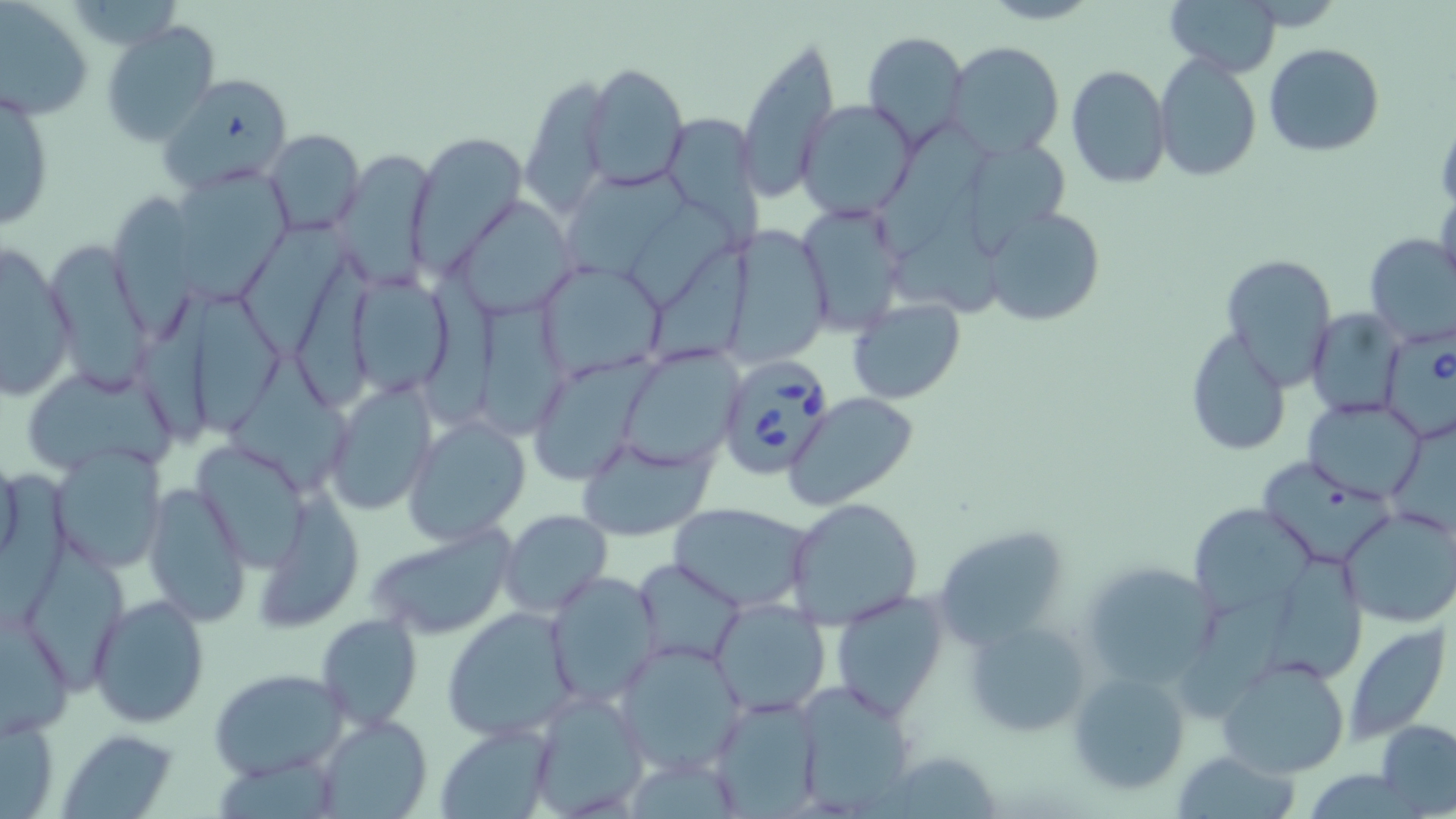
Babesia divergens-infected red blood cell locations = approximate bounding boxes as named x1/y1/x2/y2 corners in pixels: (x1=1383, y1=330, x2=1455, y2=452), (x1=715, y1=356, x2=837, y2=481)
slide-level diagnosis = Babesia divergens
image size = 1456×819 pixels
uninfected red blood cell locations = approximate bounding boxes as named x1/y1/x2/y2 corners in pixels: (x1=1164, y1=0, x2=1279, y2=74), (x1=0, y1=1, x2=93, y2=120), (x1=101, y1=20, x2=222, y2=145), (x1=862, y1=30, x2=969, y2=146), (x1=735, y1=36, x2=839, y2=202), (x1=944, y1=40, x2=1065, y2=158), (x1=1264, y1=43, x2=1385, y2=156), (x1=1154, y1=53, x2=1262, y2=183), (x1=582, y1=63, x2=689, y2=188), (x1=1066, y1=64, x2=1170, y2=189), (x1=159, y1=73, x2=293, y2=190), (x1=519, y1=80, x2=610, y2=213), (x1=0, y1=83, x2=55, y2=235), (x1=797, y1=100, x2=916, y2=219), (x1=671, y1=110, x2=769, y2=238), (x1=875, y1=121, x2=988, y2=251), (x1=263, y1=128, x2=366, y2=239), (x1=406, y1=132, x2=525, y2=274), (x1=967, y1=141, x2=1065, y2=254), (x1=329, y1=150, x2=437, y2=290), (x1=168, y1=168, x2=294, y2=300), (x1=1435, y1=182, x2=1456, y2=297), (x1=110, y1=190, x2=195, y2=340), (x1=625, y1=196, x2=739, y2=302), (x1=455, y1=197, x2=575, y2=315), (x1=984, y1=206, x2=1107, y2=329), (x1=800, y1=207, x2=905, y2=343), (x1=243, y1=210, x2=350, y2=353), (x1=719, y1=228, x2=828, y2=362), (x1=1364, y1=234, x2=1455, y2=346), (x1=1, y1=240, x2=78, y2=401), (x1=45, y1=241, x2=152, y2=389), (x1=1222, y1=253, x2=1338, y2=383), (x1=537, y1=262, x2=663, y2=381), (x1=349, y1=269, x2=454, y2=401), (x1=136, y1=289, x2=215, y2=447), (x1=194, y1=292, x2=283, y2=440), (x1=847, y1=297, x2=965, y2=404), (x1=1305, y1=309, x2=1405, y2=416), (x1=1185, y1=329, x2=1293, y2=457), (x1=229, y1=346, x2=349, y2=494), (x1=621, y1=347, x2=745, y2=468), (x1=527, y1=357, x2=654, y2=486), (x1=21, y1=364, x2=177, y2=480), (x1=323, y1=385, x2=437, y2=515), (x1=785, y1=392, x2=920, y2=511), (x1=1305, y1=397, x2=1428, y2=503), (x1=403, y1=416, x2=531, y2=544), (x1=577, y1=436, x2=713, y2=540), (x1=50, y1=446, x2=170, y2=573), (x1=196, y1=447, x2=312, y2=575), (x1=0, y1=452, x2=23, y2=570), (x1=1259, y1=456, x2=1385, y2=558), (x1=143, y1=480, x2=251, y2=626), (x1=258, y1=492, x2=367, y2=627), (x1=783, y1=496, x2=924, y2=629), (x1=668, y1=503, x2=813, y2=612), (x1=1188, y1=503, x2=1317, y2=622), (x1=1337, y1=507, x2=1456, y2=629), (x1=500, y1=509, x2=612, y2=617), (x1=929, y1=523, x2=1072, y2=646), (x1=365, y1=524, x2=517, y2=641), (x1=1269, y1=546, x2=1370, y2=678), (x1=633, y1=557, x2=747, y2=667), (x1=1080, y1=563, x2=1222, y2=689), (x1=545, y1=571, x2=663, y2=705), (x1=830, y1=589, x2=951, y2=720), (x1=88, y1=593, x2=210, y2=727), (x1=1185, y1=596, x2=1303, y2=715), (x1=709, y1=597, x2=832, y2=716), (x1=443, y1=606, x2=577, y2=742), (x1=0, y1=611, x2=76, y2=740), (x1=317, y1=613, x2=422, y2=730), (x1=969, y1=617, x2=1091, y2=737), (x1=1344, y1=621, x2=1453, y2=744), (x1=614, y1=640, x2=750, y2=776), (x1=1216, y1=656, x2=1352, y2=777), (x1=1067, y1=668, x2=1190, y2=795), (x1=210, y1=669, x2=347, y2=779), (x1=792, y1=680, x2=923, y2=813), (x1=529, y1=690, x2=649, y2=817), (x1=708, y1=695, x2=825, y2=816), (x1=1, y1=710, x2=62, y2=819), (x1=313, y1=714, x2=432, y2=818), (x1=1376, y1=720, x2=1456, y2=814), (x1=436, y1=725, x2=553, y2=817), (x1=62, y1=728, x2=179, y2=819), (x1=1170, y1=747, x2=1302, y2=819), (x1=876, y1=749, x2=1008, y2=818)
magnification = 1000x
stain = May-Grünwald-Giemsa
modality = light microscopy
preparation = thin blood smear
field of view = single